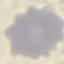

malaria status = uninfected
capture = smartphone through the microscope eyepiece
image type = automatically extracted cell patch, resized to 64 × 64 pixels
preparation = thin smear
stain = Giemsa